State which cell type is depicted.
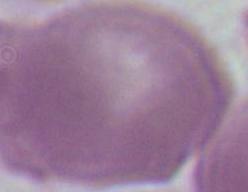
This is an erythrocyte.

modality = photomicrograph
magnification = 1000x